Report the malaria status of this cell.
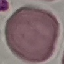
Uninfected.

Summary:
  - Stain: Giemsa
  - Preparation: thin smear
  - Image type: automatically extracted cell patch, resized to 64 × 64 pixels
  - Capture: smartphone camera at the microscope eyepiece